Outline each blood parasite and name the species.
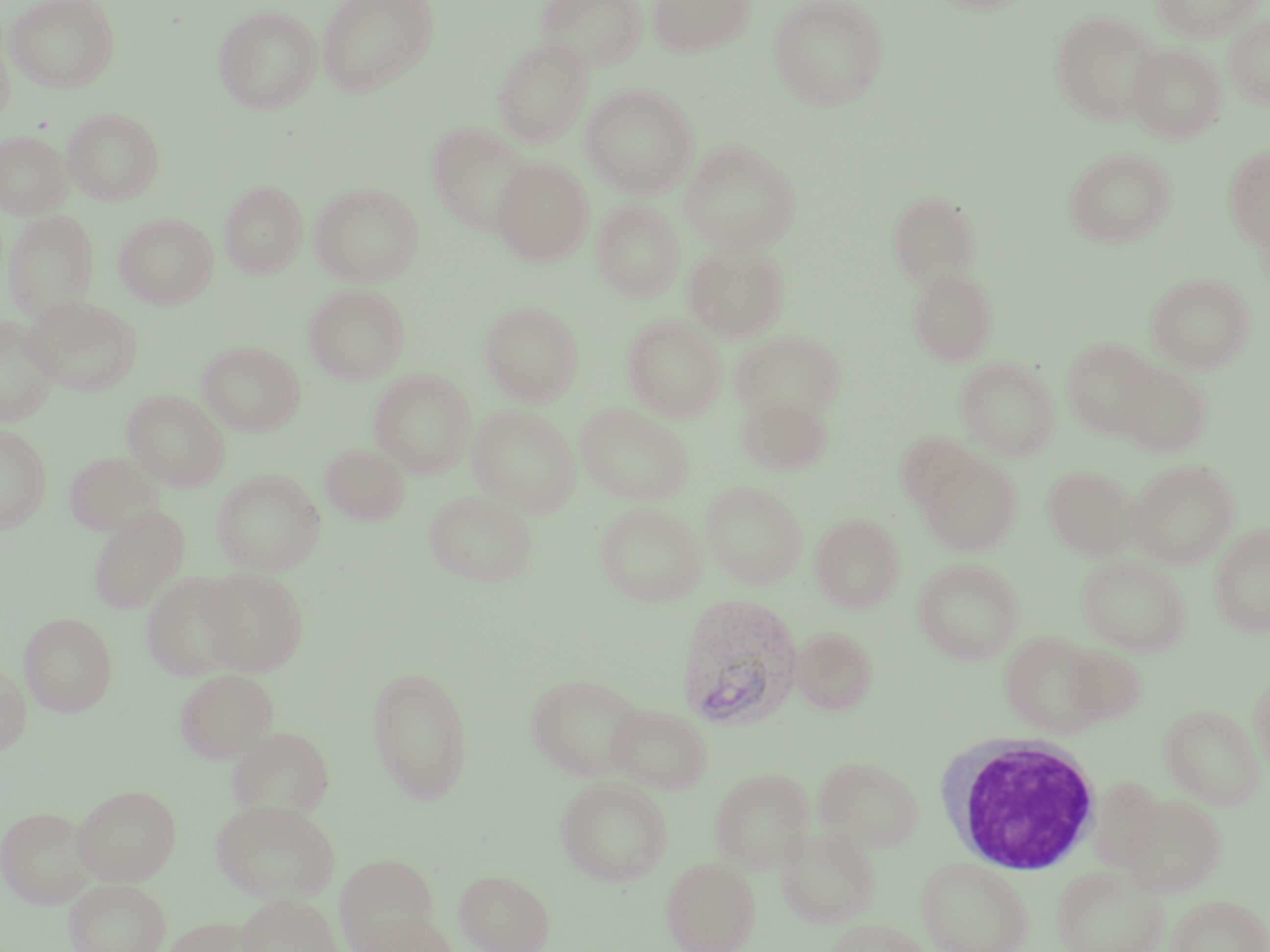
Approximate bounding boxes as (x1,y1)-(x2,y2) corner pairs in pixels.
Plasmodium vivax-infected red blood cells: (675,592)-(803,730).
No Plasmodium falciparum, Plasmodium ovale, Plasmodium malariae, Babesia divergens, or Trypanosoma brucei observed.

White blood cell locations: (934,733)-(1103,874). Uninfected red blood cell locations: (4,0)-(121,93), (316,0)-(439,98), (535,0)-(648,72), (648,0)-(754,57), (768,0)-(889,110), (1150,0)-(1262,42), (213,4)-(323,115), (1050,9)-(1163,125), (1224,15)-(1270,109), (0,24)-(14,128), (493,37)-(593,147), (1127,43)-(1226,143), (580,82)-(700,199), (63,106)-(165,205), (426,121)-(536,235), (0,130)-(73,219), (679,139)-(801,254), (1064,148)-(1175,247), (1224,148)-(1270,249), (491,157)-(593,266), (219,181)-(307,279), (309,182)-(424,287), (886,191)-(982,290), (592,199)-(684,302), (2,209)-(100,323), (113,213)-(219,309), (683,240)-(790,343), (907,269)-(997,366), (1146,272)-(1255,374), (303,283)-(410,385), (23,296)-(143,396), (480,301)-(584,407), (622,315)-(727,421), (0,316)-(61,426), (730,330)-(845,422), (1062,338)-(1158,439), (197,341)-(305,436), (956,356)-(1059,461), (1116,362)-(1212,457), (369,368)-(476,478), (122,389)-(230,492), (736,393)-(832,475), (575,403)-(695,506), (468,405)-(580,517), (0,423)-(51,533), (895,433)-(983,514), (320,443)-(410,524), (916,451)-(1022,557), (64,452)-(167,538), (1128,459)-(1240,569), (1043,465)-(1138,561), (213,468)-(325,576), (701,480)-(807,589), (424,489)-(538,587), (595,502)-(708,606), (88,506)-(189,614), (810,513)-(905,613), (1208,522)-(1270,638), (1078,555)-(1191,657), (912,558)-(1024,664), (197,568)-(309,675), (141,570)-(244,681), (18,611)-(118,716), (790,627)-(878,715), (1000,631)-(1106,737), (1060,644)-(1147,726), (0,662)-(31,755), (367,665)-(474,804), (175,669)-(278,764), (525,672)-(649,781), (1249,673)-(1270,779), (606,703)-(713,795), (1158,703)-(1265,811), (225,726)-(336,818), (812,756)-(924,852), (708,768)-(815,873), (555,775)-(673,887), (1087,777)-(1165,869), (73,784)-(182,885), (1120,794)-(1226,898), (213,799)-(339,902), (0,806)-(98,908), (776,825)-(880,928), (335,854)-(437,950), (662,857)-(761,952), (917,857)-(1033,952), (1052,864)-(1169,952), (454,869)-(555,952), (63,878)-(171,952), (237,892)-(341,952), (1166,894)-(1270,952), (360,914)-(459,952), (163,916)-(263,952), (826,918)-(933,952). Slide-level diagnosis: Plasmodium vivax. May-Grünwald-Giemsa-stained preparation. Light microscopy. Single field of view. Image is 1270×952 pixels. Thin blood smear. Captured at 1000x magnification.